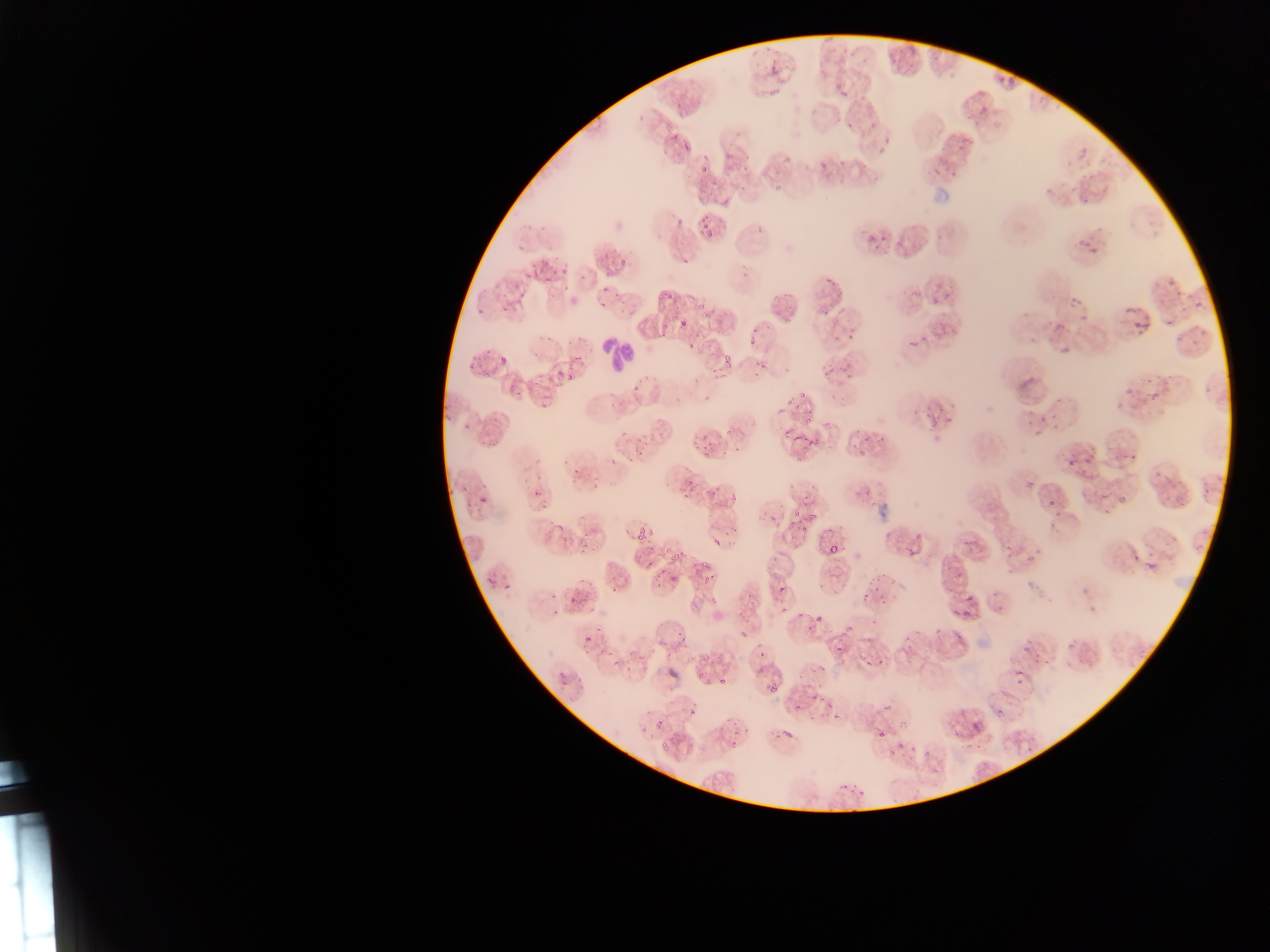
Approximate bounding boxes as left top right bottom in pixels.
Summary:
  - Leukocyte locations: 598 335 637 376
  - Plasmodium parasite locations (subset; some below the resolvable size): 769 65 777 74; 1005 75 1015 83; 834 84 842 90; 839 92 847 97; 669 133 678 138; 681 133 693 150; 703 150 707 158; 818 162 828 171; 699 163 709 172; 1081 197 1089 205; 675 215 685 223; 536 223 547 230; 705 232 713 236; 866 233 875 241; 882 236 888 244; 1079 242 1089 248; 1088 246 1099 255; 603 253 611 258; 619 258 628 266; 529 263 539 269; 552 267 558 275; 561 267 569 274; 579 270 585 282; 525 272 536 282; 606 272 616 278; 544 274 553 280; 825 274 835 287; 600 285 608 291; 516 289 526 299; 615 289 622 299; 665 290 673 301; 945 291 949 299; 1184 291 1207 319; 1173 292 1181 300; 655 293 664 304; 934 294 939 305; 1069 296 1077 307; 598 301 606 309; 1120 301 1153 339; 502 305 509 313; 695 305 703 311; 477 306 484 315; 671 311 677 324; 699 311 707 319; 786 315 792 323; 1163 318 1172 330; 1045 320 1052 328; 1055 321 1069 330; 848 328 854 341; 938 328 946 337; 833 330 844 342; 749 338 758 346; 909 339 918 350; 686 341 696 348; 1058 342 1069 354; 486 346 492 354; 570 355 584 363; 722 355 730 367; 473 356 481 362; 499 356 510 362; 759 362 768 371; 466 364 473 372; 710 368 719 374; 825 368 832 377; 481 371 489 378; 555 373 563 379; 567 373 572 382; 532 380 540 391; 554 382 562 391; 508 383 516 390; 1202 383 1209 396; 632 387 640 395; 1122 387 1133 397; 516 389 524 398; 533 390 543 397; 1149 391 1157 398; 798 392 806 402; 1053 396 1061 405; 538 397 549 411; 787 397 794 406; 606 403 614 409; 776 407 783 415; 444 412 451 422; 1051 412 1061 425; 945 415 954 425; 1039 416 1046 424; 804 417 814 423; 821 417 832 428; 1025 419 1031 427; 464 420 473 429; 929 424 938 433; 781 427 789 436; 853 428 861 433; 619 429 627 440; 802 432 810 443; 791 434 800 442; 874 434 885 447; 489 436 503 447; 477 438 485 446; 702 443 712 450; 644 444 653 451; 722 448 731 456; 1122 448 1139 462; 1069 450 1080 459; 636 451 645 458; 1085 453 1095 465; 627 454 634 462; 608 455 617 464; 794 457 803 463; 564 459 571 467; 1153 468 1166 479; 1026 477 1040 486; 685 481 693 485; 591 483 599 490; 1200 485 1210 497; 864 486 874 496; 710 488 717 497; 682 489 689 499; 532 491 540 496; 729 491 740 502; 1101 491 1110 500; 476 492 493 510; 1045 493 1066 517; 1164 494 1172 502; 1118 495 1125 506; 1179 498 1187 506; 541 504 549 509; 792 509 802 517; 770 513 776 522; 807 513 818 521; 796 521 804 525; 552 523 561 531; 826 523 835 533; 730 524 737 532; 800 525 811 532; 624 528 634 535; 883 529 889 537; 634 530 645 543; 916 530 923 539; 960 531 972 546; 711 535 720 547; 577 539 589 555; 1004 539 1012 550; 648 544 656 550; 663 545 671 552; 828 545 839 553; 905 548 914 559; 1130 549 1138 561; 668 550 680 561; 647 555 655 565; 1142 556 1160 576; 1022 557 1030 567; 701 558 711 569; 658 566 666 574; 701 572 713 584; 955 572 964 582; 484 573 496 584; 866 577 876 585; 656 580 663 588; 502 583 514 591; 874 583 880 593; 777 585 785 593; 611 587 620 593; 549 592 557 598; 860 592 866 602; 570 594 579 605; 710 594 719 606; 745 594 753 601; 953 595 981 625; 879 598 886 606; 552 607 562 615; 795 612 803 619; 846 623 852 631; 804 627 813 633; 676 628 686 639; 584 633 592 644; 680 635 691 642; 656 638 664 646; 837 644 843 653; 1023 645 1029 654; 758 648 766 659; 607 650 616 658; 698 652 708 661; 1033 652 1040 663; 875 655 884 666; 1045 655 1054 666; 610 660 620 667; 863 661 873 666; 814 665 827 673; 1011 667 1023 689; 699 669 707 678; 556 670 567 678; 719 674 728 683; 768 685 777 695; 810 694 816 703; 819 697 827 703; 788 699 805 710; 825 700 833 711; 875 702 892 713; 687 706 701 715; 996 708 1002 716; 830 711 844 721; 726 714 733 723; 967 718 984 737; 653 720 663 729; 778 724 797 738; 732 727 741 736; 877 728 885 739; 728 738 736 748; 894 739 905 750; 661 741 672 750; 908 745 915 754; 923 745 929 757; 888 747 896 756; 840 777 849 786; 853 782 867 794 | approximate x y pixel centers of objects too small to bound: 1072 190; 706 226; 685 259; 1168 283; 565 287; 827 312; 1083 321; 682 324; 755 330; 1177 339; 923 340; 1194 343; 757 365; 755 376; 849 376; 706 399; 621 405; 798 406; 915 414; 925 416; 728 431; 641 440; 813 441; 864 442; 696 448; 738 452; 1070 465; 575 472; 573 483; 464 488; 469 503; 673 579; 995 595; 783 607; 818 618; 599 629; 601 652; 563 682; 746 730
  - Field of view: single
  - Preparation: thin blood film
  - Country: Ghana
  - Image size: 1270×952 pixels
  - Capture: mobile-phone photograph through a microscope